Locate every uninfected red blood cell.
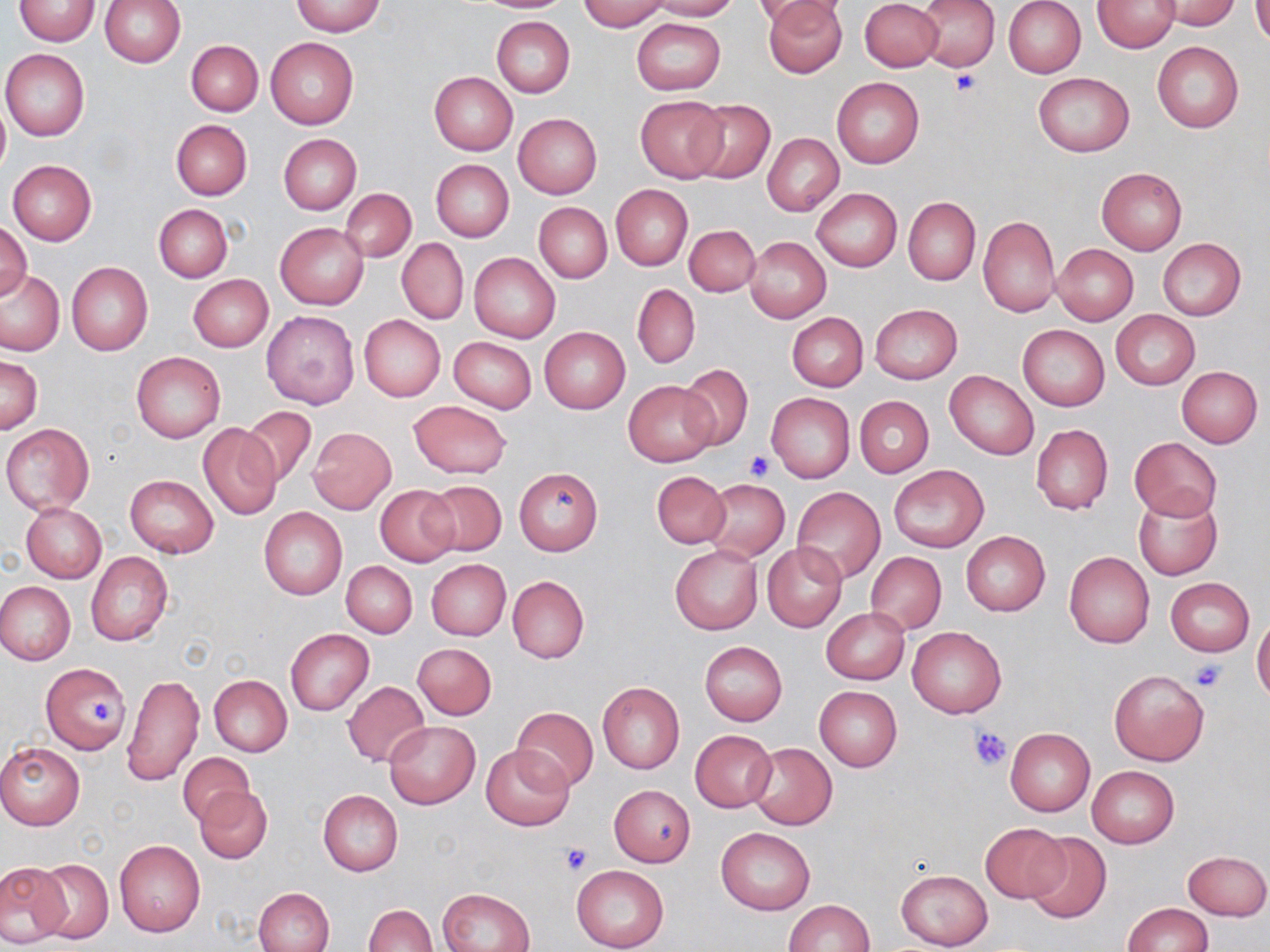

Approximate bounding boxes as [x1, y1, x2, y2] in pixels.
Uninfected red blood cells: [100, 0, 186, 68], [465, 0, 576, 13], [576, 0, 671, 31], [647, 0, 740, 20], [753, 0, 848, 28], [762, 0, 847, 77], [861, 0, 942, 71], [918, 0, 999, 69], [1003, 0, 1086, 78], [1093, 0, 1179, 52], [1156, 0, 1242, 29], [14, 1, 100, 45], [290, 1, 384, 36], [1251, 2, 1270, 47], [492, 16, 575, 98], [631, 18, 725, 94], [266, 38, 357, 129], [186, 40, 263, 117], [1152, 42, 1243, 132], [1, 49, 90, 140], [430, 72, 517, 155], [1033, 72, 1135, 157], [832, 77, 924, 168], [635, 94, 729, 182], [691, 97, 774, 184], [0, 102, 9, 180], [514, 113, 602, 198], [171, 120, 252, 199], [762, 133, 843, 216], [278, 134, 361, 215], [7, 159, 97, 245], [431, 159, 514, 242], [1097, 167, 1187, 254], [611, 184, 693, 269], [812, 187, 902, 272], [341, 189, 416, 263], [903, 197, 980, 286], [534, 202, 612, 283], [154, 204, 232, 282], [978, 215, 1060, 317], [1, 219, 32, 305], [275, 222, 369, 310], [684, 223, 760, 296], [744, 236, 831, 323], [1158, 238, 1246, 321], [397, 239, 469, 324], [1052, 244, 1139, 324], [469, 252, 560, 342], [66, 262, 152, 355], [1, 268, 66, 357], [188, 275, 271, 352], [632, 283, 700, 369], [869, 304, 963, 385], [261, 310, 361, 411], [1111, 310, 1200, 389], [788, 312, 868, 392], [358, 315, 445, 402], [1018, 324, 1109, 411], [539, 327, 630, 413], [448, 337, 537, 412], [132, 352, 225, 442], [0, 354, 42, 434], [676, 365, 754, 450], [1176, 367, 1262, 448], [944, 370, 1039, 460], [624, 380, 717, 466], [767, 392, 855, 484], [854, 396, 933, 477], [407, 400, 511, 478], [242, 407, 317, 488], [199, 422, 284, 519], [3, 423, 94, 515], [1031, 423, 1114, 516], [309, 427, 396, 514], [1130, 437, 1222, 521], [889, 465, 989, 550], [515, 467, 603, 555], [652, 471, 730, 547], [125, 475, 218, 558], [703, 479, 790, 560], [423, 480, 507, 557], [375, 486, 460, 566], [791, 487, 886, 583], [1133, 492, 1222, 581], [21, 503, 106, 582], [259, 507, 347, 600], [961, 531, 1050, 616], [762, 543, 847, 633], [670, 545, 762, 634], [865, 551, 946, 636], [1064, 551, 1154, 648], [86, 552, 173, 645], [425, 559, 511, 640], [342, 561, 417, 637], [507, 576, 589, 665], [1166, 578, 1254, 656], [0, 582, 75, 665], [821, 608, 911, 685], [1252, 614, 1270, 703], [907, 625, 1007, 718], [285, 629, 374, 715], [699, 641, 787, 725], [412, 643, 497, 720], [42, 663, 129, 756], [1109, 669, 1209, 766], [122, 673, 205, 787], [210, 676, 292, 756], [343, 681, 430, 767], [598, 682, 684, 773], [814, 685, 902, 771], [511, 706, 597, 793], [384, 720, 479, 808], [1006, 727, 1095, 817], [689, 730, 777, 813], [0, 742, 85, 829], [746, 742, 837, 832], [481, 744, 575, 831], [178, 753, 255, 827], [1087, 766, 1179, 848], [194, 784, 271, 864], [609, 784, 695, 866], [317, 789, 403, 875], [981, 822, 1068, 903], [716, 827, 815, 915], [1024, 832, 1110, 924], [114, 839, 206, 935], [1183, 850, 1269, 920], [34, 859, 113, 944], [0, 862, 70, 945], [571, 866, 669, 952], [895, 869, 991, 949], [254, 887, 334, 952], [439, 888, 536, 952], [784, 899, 873, 952], [1122, 903, 1213, 951], [364, 904, 437, 952].

Platelet locations: [951, 69, 983, 95], [744, 449, 775, 479], [1188, 661, 1227, 693], [87, 703, 116, 726], [969, 728, 1011, 771], [559, 842, 593, 875]. Slide-level diagnosis: no evidence of blood parasites. May-Grünwald-Giemsa-stained preparation. Image is 1270×952 pixels. Thin blood film. Optical microscopy. One field of a larger specimen. 1000x magnification.